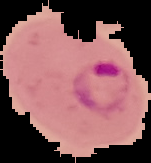
result = Plasmodium parasites identified
image size = 151×163 pixels
image type = segmented cell region with the area outside set to black
preparation = thin blood smear